Describe the morphology of the red blood cells.
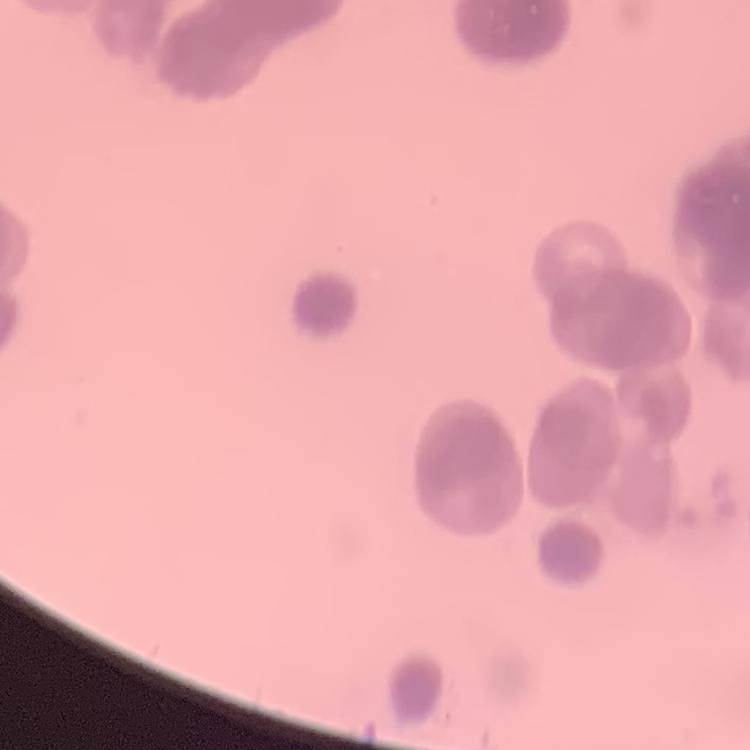
They show rouleaux formation.

One tile cut from a larger photomicrograph. Thin blood film. Stained with either Field's or Giemsa.